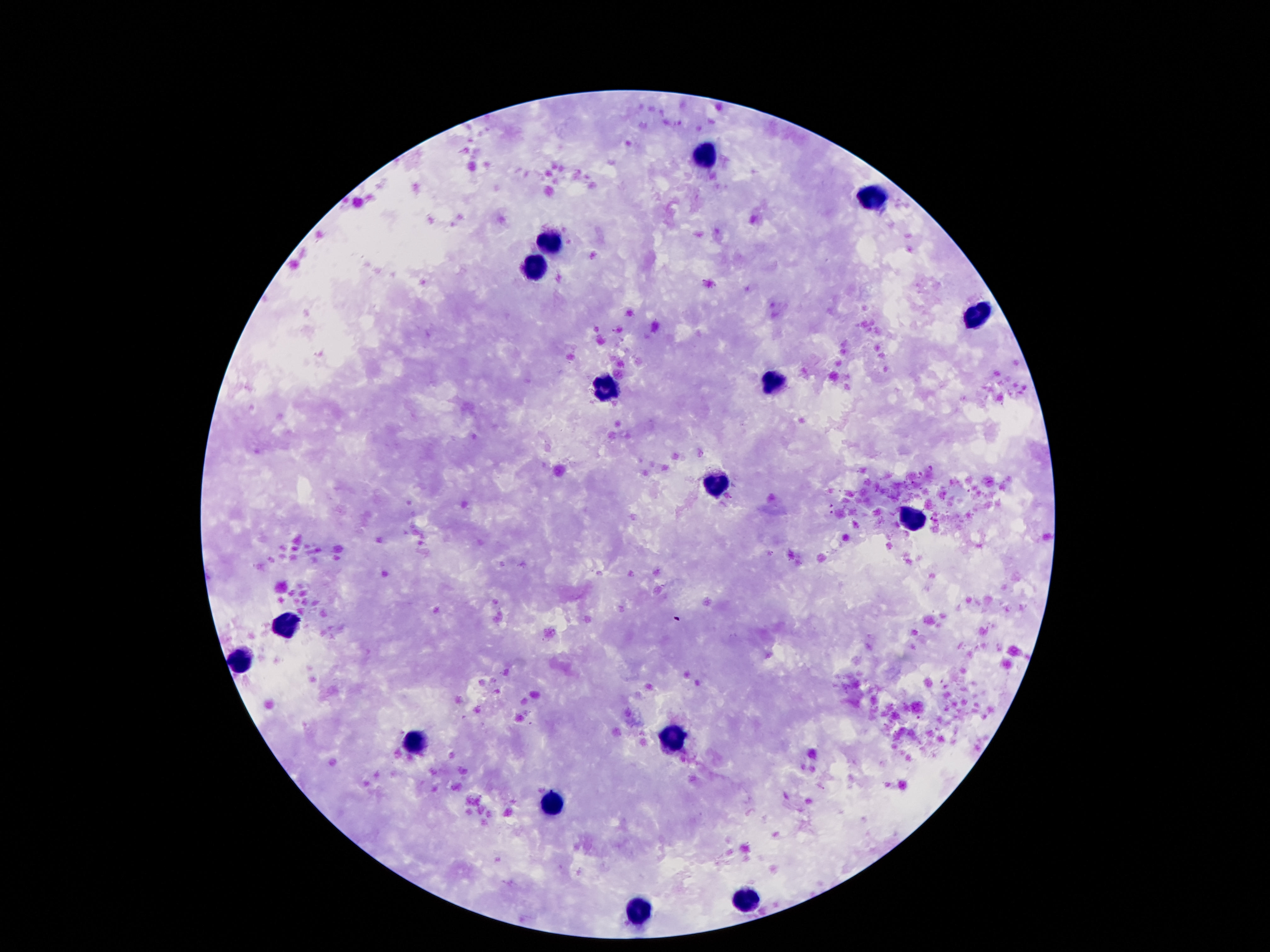
Approximate object centers, in pixels from the top-left corner.
Summary:
  - Leukocyte locations: (x=704, y=152), (x=870, y=197), (x=550, y=241), (x=531, y=270), (x=975, y=310), (x=775, y=379), (x=607, y=390), (x=714, y=486), (x=914, y=521), (x=286, y=625), (x=242, y=659), (x=672, y=739), (x=412, y=743), (x=552, y=802), (x=748, y=903), (x=636, y=910)
  - Magnification: 100x
  - Image size: 1270×952 pixels
  - Preparation: thick peripheral-blood smear
  - Stain: Giemsa
  - Patient malaria status: uninfected
  - Capture: smartphone camera through the microscope eyepiece
  - Field of view: one from this slide